Assess this cell for malaria.
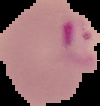

It is parasitized.

Image is 100×106 pixels. The area outside the segmented cell region is set to black. From a thin blood smear.